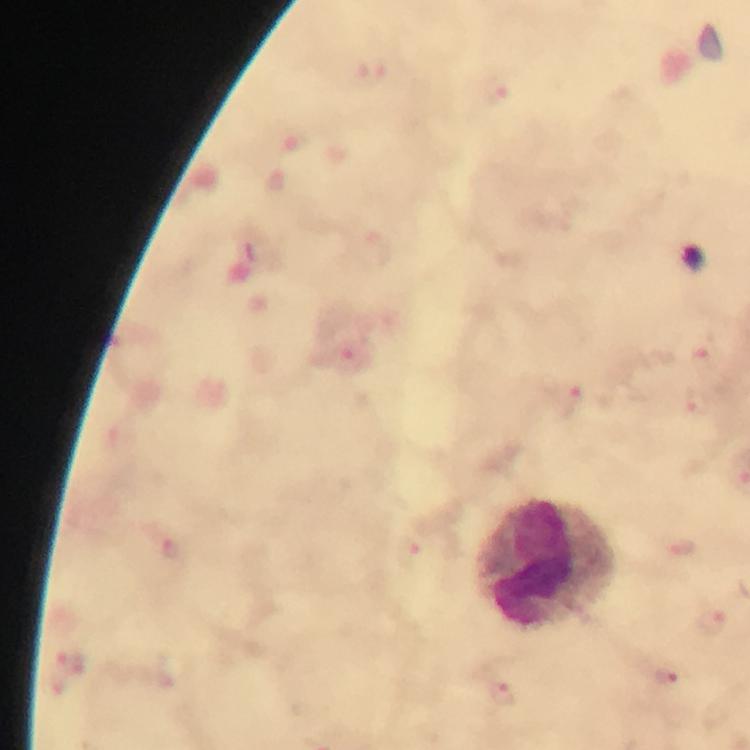 Approximate centers as [x, y] in pixels. Leukocyte locations: [549, 566]. Malaria parasite locations: [373, 73], [494, 88], [356, 360], [703, 361], [566, 398], [696, 404], [684, 546], [710, 618], [72, 660], [668, 677], [503, 694]. Giemsa-stained preparation. Smartphone photograph taken through a microscope. Thick blood film. From a diagnostic examination for malaria. At 100x magnification. Immersion oil was used. A crop from one field of view. Image is 750×750 pixels.